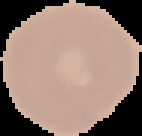

Result: no malaria parasites seen. Image is 142×136 pixels. From a thin blood smear. Segmented cell region on a black background.